Describe the morphology of the erythrocytes.
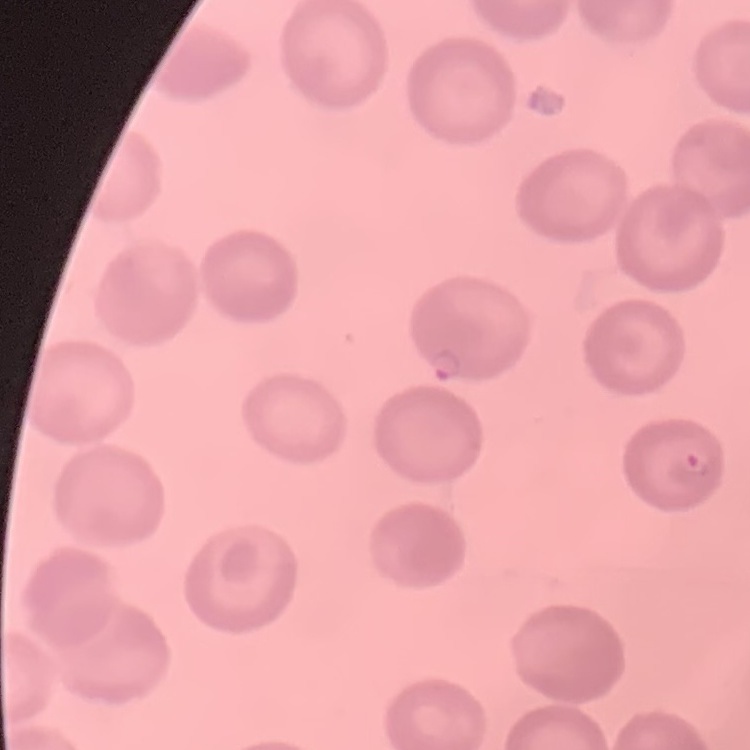
They show no rouleaux formation.

Summary:
  - Stain: Field's or Giemsa
  - Preparation: thin blood smear
  - Image type: one tile cut from a larger photomicrograph